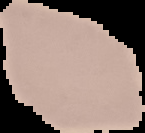
Image is 145×133 pixels. Cell region segmented out of the field of view; the surrounding area is masked to black. From a thin blood film. Malaria status: uninfected.